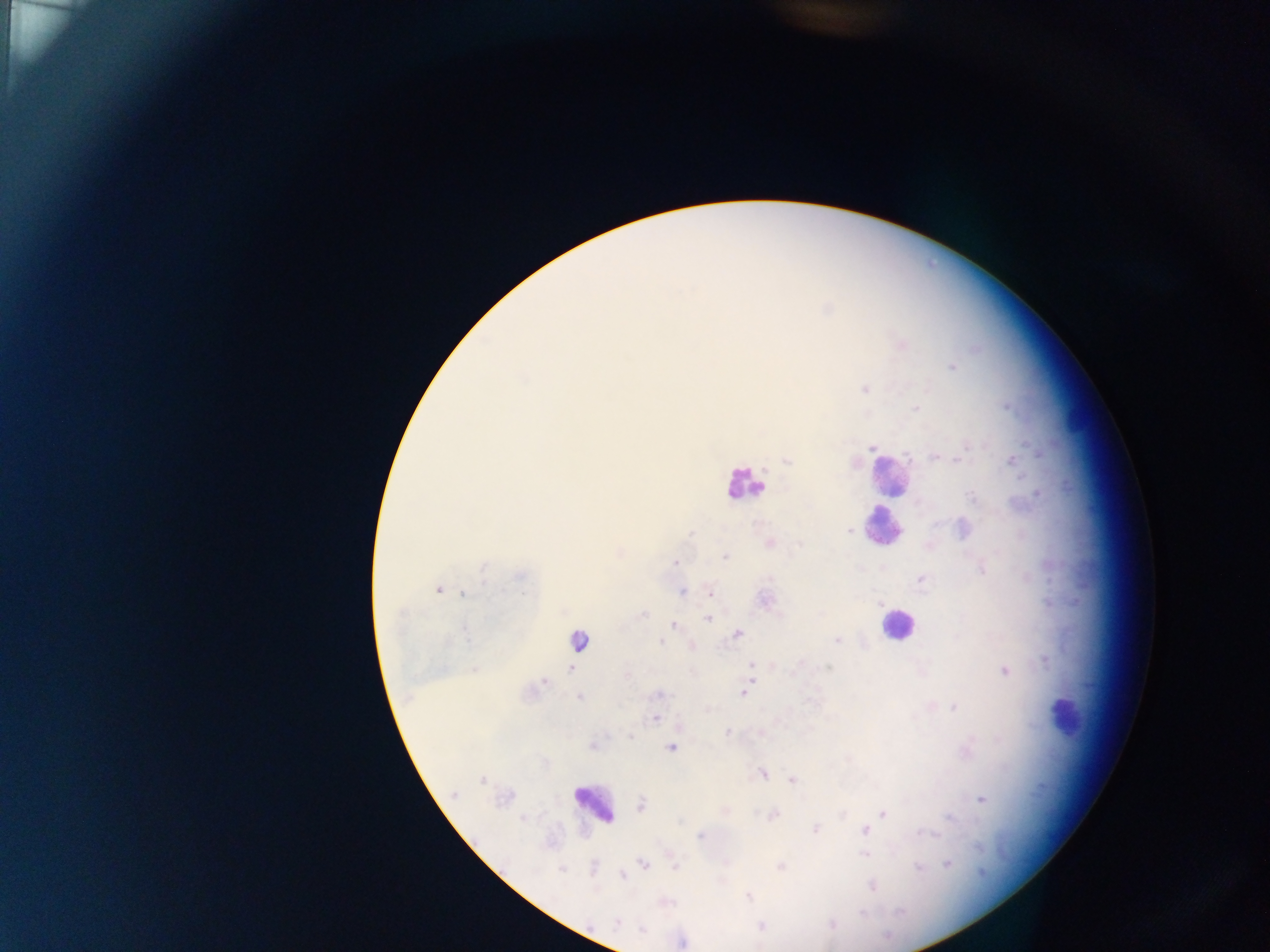

Approximate centers as [x, y] in pixels.
Summary:
  - Leukocyte locations: [888, 480], [744, 483], [883, 527], [897, 626], [578, 640], [1065, 716], [593, 803]
  - Plasmodium parasite locations: [901, 344], [951, 367], [865, 389], [916, 408], [936, 456], [787, 460], [1011, 460], [962, 529], [850, 530], [770, 543], [726, 558], [676, 562], [982, 567], [922, 579], [438, 590], [682, 591], [710, 592], [463, 594], [764, 599], [642, 615], [708, 617], [674, 625], [737, 634], [837, 640], [660, 641], [691, 646], [751, 666], [1004, 670], [542, 681], [744, 692], [659, 694], [579, 697], [955, 707], [654, 718], [680, 726], [726, 734], [593, 745], [672, 747], [762, 773], [793, 781], [980, 798], [640, 804], [884, 812], [773, 815], [815, 829], [865, 829], [700, 836], [864, 854], [948, 862], [643, 865], [676, 867], [781, 867], [621, 876], [748, 896], [760, 926]
  - Field of view: single
  - Image size: 1270×952 pixels
  - Capture: mobile-phone photograph through a microscope
  - Preparation: thick blood film
  - Country: Ghana